Name the parasite shown.
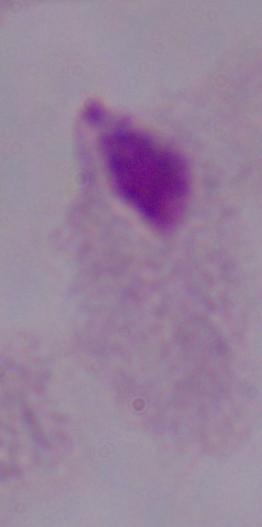

A trichomonad.

modality = photomicrograph
magnification = 1000x